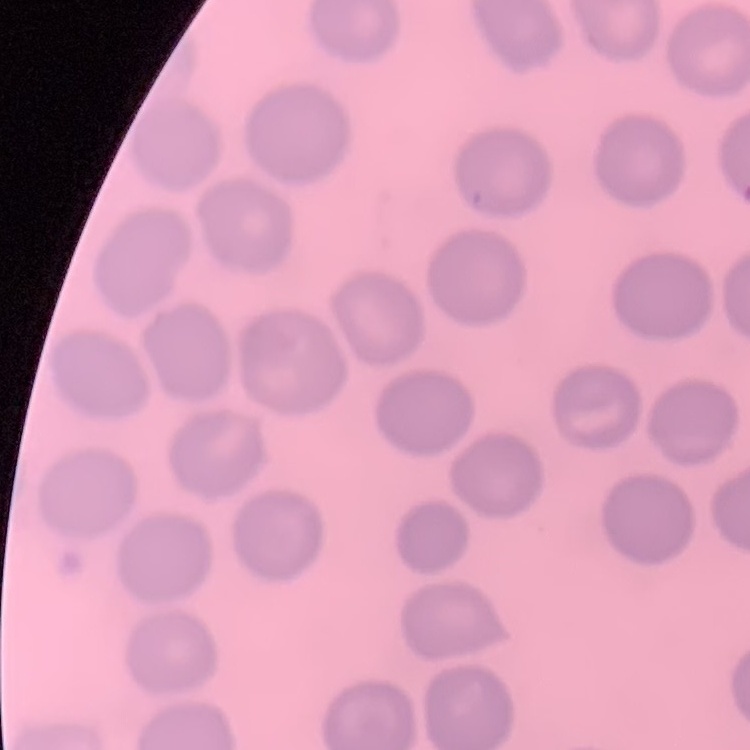

red blood cell morphology = no rouleaux formation
image type = one tile cut from a larger photomicrograph
stain = Field's or Giemsa
preparation = thin blood film